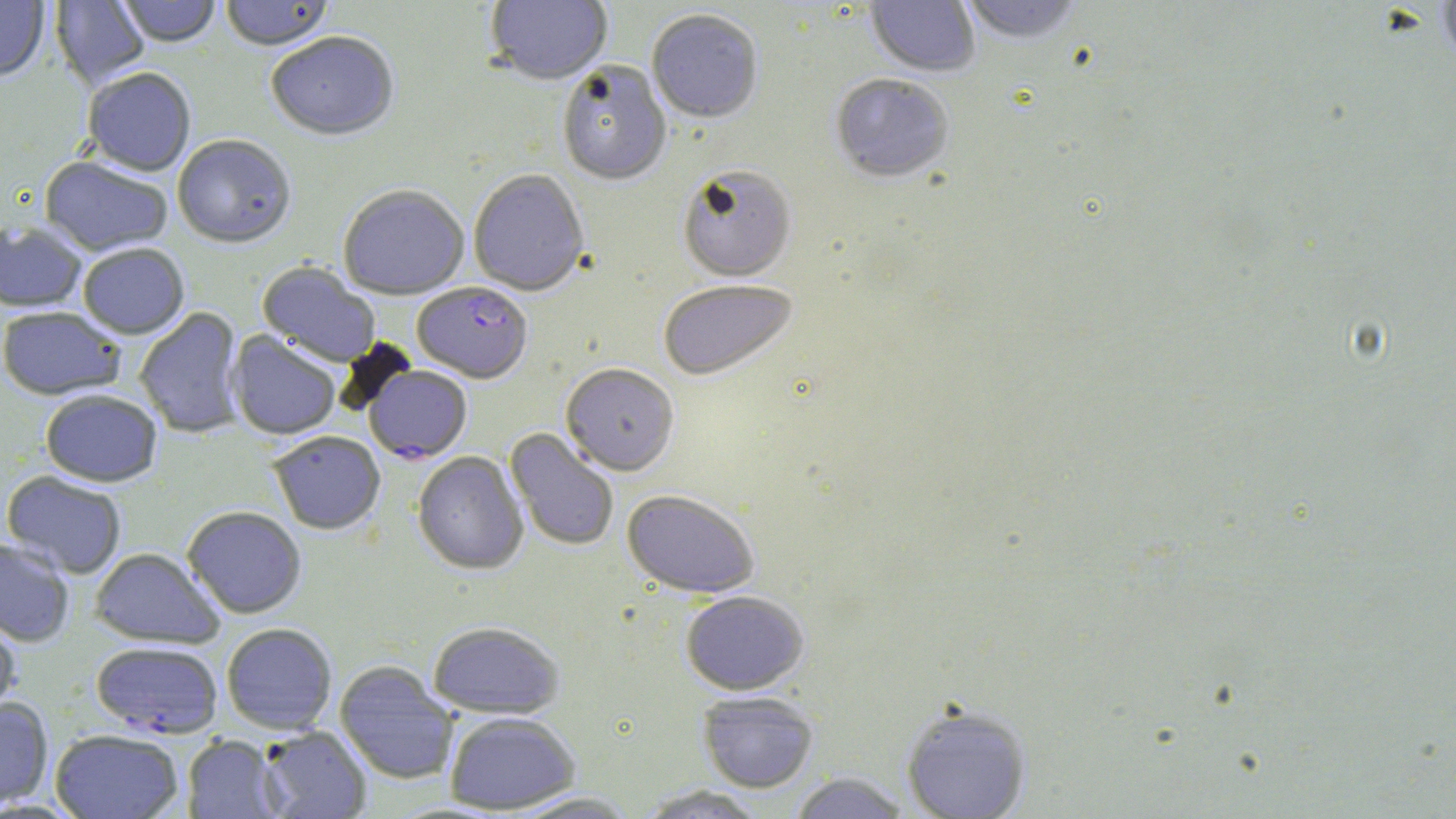
slide-level diagnosis = Plasmodium falciparum
field of view = single
uninfected red blood cell locations = approximate bounding boxes as [x1, y1, x2, y2] in pixels: [116, 0, 221, 49], [220, 0, 335, 53], [485, 0, 613, 88], [865, 0, 980, 79], [957, 0, 1086, 46], [0, 1, 49, 83], [50, 1, 150, 90], [1436, 1, 1456, 66], [647, 12, 763, 126], [266, 34, 399, 144], [557, 62, 671, 189], [83, 70, 196, 178], [830, 75, 954, 186], [172, 137, 296, 252], [39, 157, 173, 258], [678, 167, 796, 283], [468, 170, 589, 298], [338, 186, 469, 302], [0, 222, 86, 313], [78, 245, 189, 341], [257, 261, 380, 369], [658, 282, 799, 384], [0, 308, 125, 401], [134, 308, 247, 439], [227, 331, 341, 441], [560, 365, 679, 479], [41, 391, 162, 488], [505, 428, 619, 552], [269, 433, 385, 536], [412, 452, 528, 576], [1, 471, 127, 580], [622, 490, 759, 599], [182, 507, 306, 619], [0, 539, 74, 648], [89, 548, 224, 649], [681, 592, 809, 695], [0, 615, 20, 721], [427, 622, 564, 720], [221, 624, 337, 735], [334, 662, 460, 784], [696, 691, 818, 793], [0, 697, 54, 808], [901, 703, 1032, 819], [445, 713, 580, 814], [258, 726, 372, 818], [51, 730, 184, 819], [183, 735, 283, 818], [789, 772, 910, 818], [635, 785, 768, 818], [505, 792, 642, 818]
preparation = thin blood smear
stain = May-Grünwald-Giemsa
magnification = 1000x
Plasmodium falciparum-infected red blood cell locations = approximate bounding boxes as [x1, y1, x2, y2] in pixels: [413, 284, 532, 385], [364, 367, 472, 465], [92, 642, 222, 739]
modality = optical microscopy
image size = 1456×819 pixels